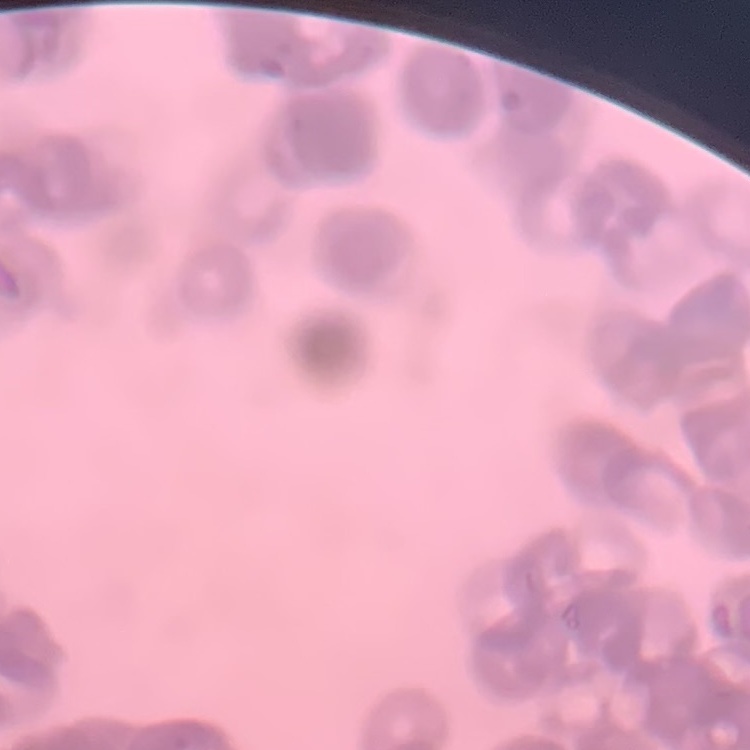

The erythrocytes show rouleaux formation. Thin peripheral smear. Field's or Giemsa stain. Square crop of a larger photomicrograph.